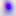

Photomicrograph. Captured at 400x magnification. Toxoplasma gondii is seen.